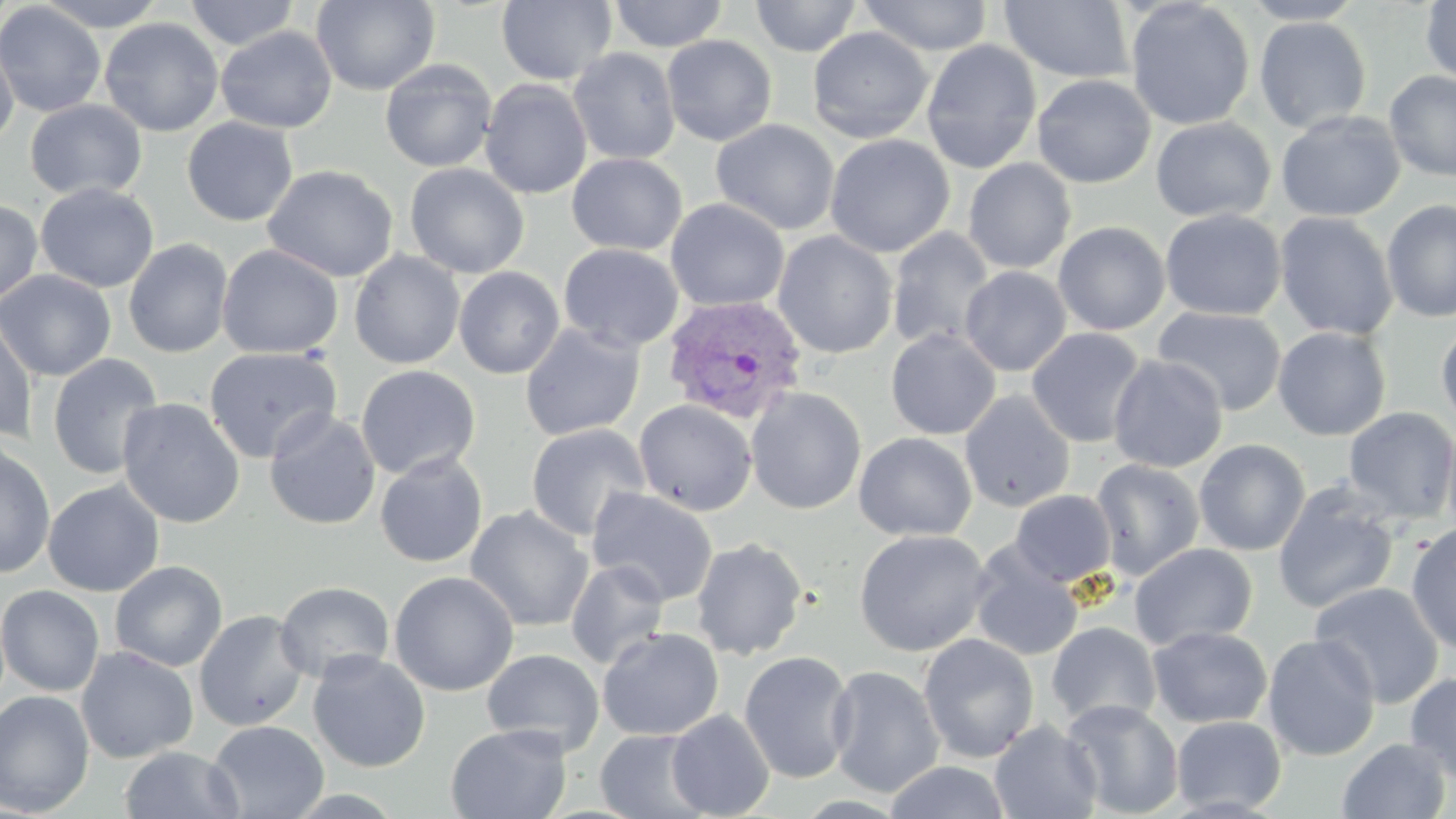
slide-level diagnosis = Plasmodium vivax
field of view = single
uninfected red blood cell locations = approximate bounding boxes as [x1, y1, x2, y2] in pixels: [38, 0, 168, 30], [184, 0, 300, 50], [311, 0, 440, 95], [608, 0, 728, 52], [750, 0, 863, 58], [858, 0, 994, 57], [999, 0, 1135, 84], [1125, 0, 1255, 130], [1240, 0, 1367, 25], [496, 1, 617, 86], [1420, 1, 1455, 86], [0, 2, 106, 117], [1254, 16, 1372, 133], [100, 17, 224, 137], [215, 26, 338, 133], [807, 27, 934, 144], [661, 35, 778, 146], [0, 37, 19, 149], [921, 39, 1042, 174], [567, 47, 681, 165], [379, 59, 497, 173], [1384, 71, 1456, 182], [1032, 73, 1156, 188], [480, 79, 592, 199], [25, 99, 147, 201], [1275, 110, 1406, 222], [182, 116, 298, 226], [1150, 117, 1276, 222], [711, 119, 840, 236], [825, 134, 955, 258], [566, 152, 687, 256], [962, 158, 1076, 274], [405, 163, 529, 279], [262, 164, 398, 282], [35, 182, 159, 293], [666, 198, 789, 312], [1381, 199, 1456, 323], [0, 200, 43, 307], [1160, 208, 1286, 321], [1274, 211, 1398, 341], [1053, 221, 1171, 336], [887, 227, 996, 352], [773, 231, 898, 359], [123, 238, 234, 359], [558, 243, 684, 352], [217, 244, 343, 359], [350, 251, 465, 369], [960, 266, 1071, 376], [454, 267, 564, 379], [0, 270, 116, 382], [1152, 306, 1287, 416], [0, 310, 38, 443], [1436, 320, 1456, 432], [520, 322, 645, 441], [1272, 326, 1392, 441], [1026, 328, 1147, 448], [886, 329, 1001, 440], [873, 330, 987, 543], [203, 346, 341, 464], [46, 353, 164, 481], [1108, 354, 1228, 473], [356, 364, 480, 480], [746, 387, 866, 515], [959, 390, 1075, 512], [117, 398, 246, 529], [633, 399, 757, 516], [1343, 406, 1456, 525], [264, 409, 382, 531], [1441, 421, 1456, 545], [525, 424, 651, 542], [853, 432, 977, 542], [1193, 439, 1311, 556], [0, 443, 56, 579], [374, 452, 488, 568], [1091, 459, 1205, 580], [43, 480, 165, 597], [1272, 482, 1401, 614], [586, 487, 719, 606], [1010, 490, 1117, 587], [464, 506, 594, 632], [1406, 523, 1456, 655], [854, 529, 992, 657], [691, 537, 808, 660], [1129, 543, 1258, 651], [970, 546, 1084, 661], [566, 559, 671, 670], [110, 561, 227, 672], [389, 571, 519, 697], [274, 581, 395, 684], [1309, 582, 1445, 709], [0, 584, 105, 697], [194, 610, 309, 731], [1047, 622, 1162, 729], [1147, 625, 1272, 728], [597, 627, 724, 741], [1148, 628, 1379, 746], [918, 633, 1039, 763], [1262, 633, 1381, 761], [76, 646, 199, 763], [481, 649, 605, 756], [307, 651, 431, 773], [738, 651, 856, 783], [826, 665, 945, 798], [1405, 671, 1456, 786], [0, 690, 95, 816], [1061, 698, 1184, 818], [666, 709, 775, 818], [1171, 715, 1287, 815], [207, 719, 328, 819], [989, 719, 1102, 819], [445, 723, 572, 818], [595, 728, 712, 818], [1337, 737, 1452, 819], [119, 746, 244, 818], [883, 761, 1013, 819]
Plasmodium vivax-infected red blood cell locations = approximate bounding boxes as [x1, y1, x2, y2] in pixels: [661, 295, 808, 425]
magnification = 1000x
image size = 1456×819 pixels
stain = May-Grünwald-Giemsa
modality = light microscopy
preparation = thin blood smear